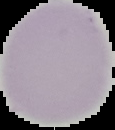 Image is 115×130 pixels. Malaria status: uninfected. Segmented cell region on a black background. From a thin blood smear.